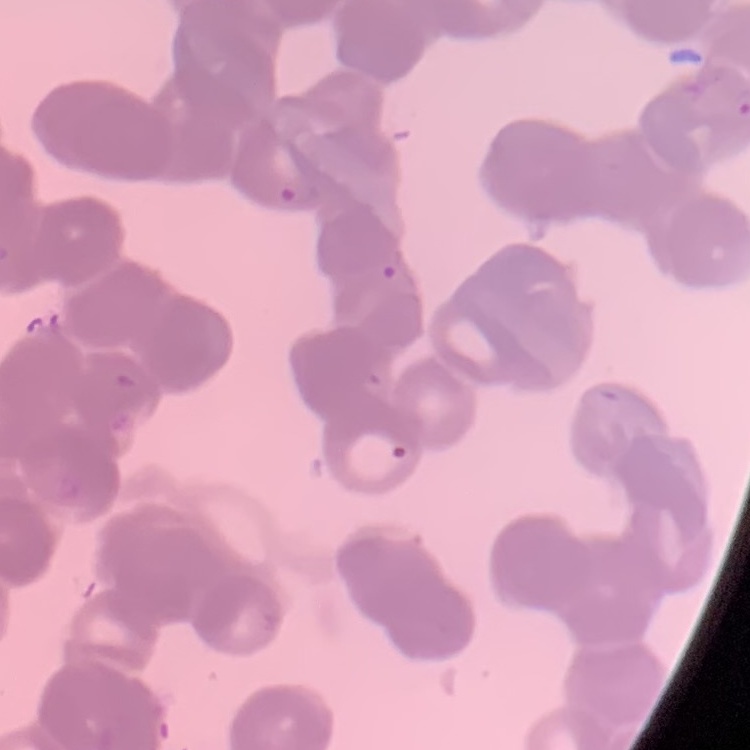

Summary:
  - Erythrocyte morphology: rouleaux formation
  - Preparation: thin peripheral smear
  - Image type: square crop of a larger photomicrograph
  - Stain: Field's or Giemsa